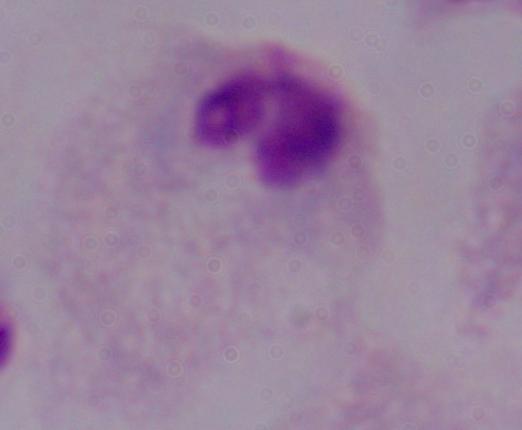 Photomicrograph. 1000x magnification. A trichomonad is seen.